Name the parasite shown.
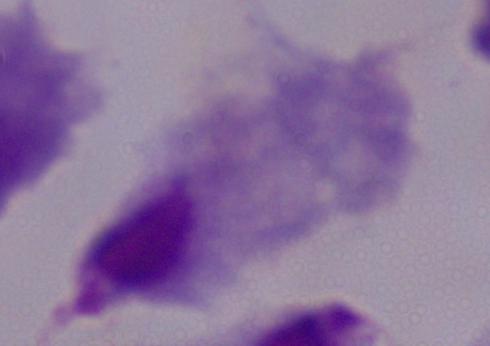

This is a trichomonad.

magnification = 1000x
modality = micrograph